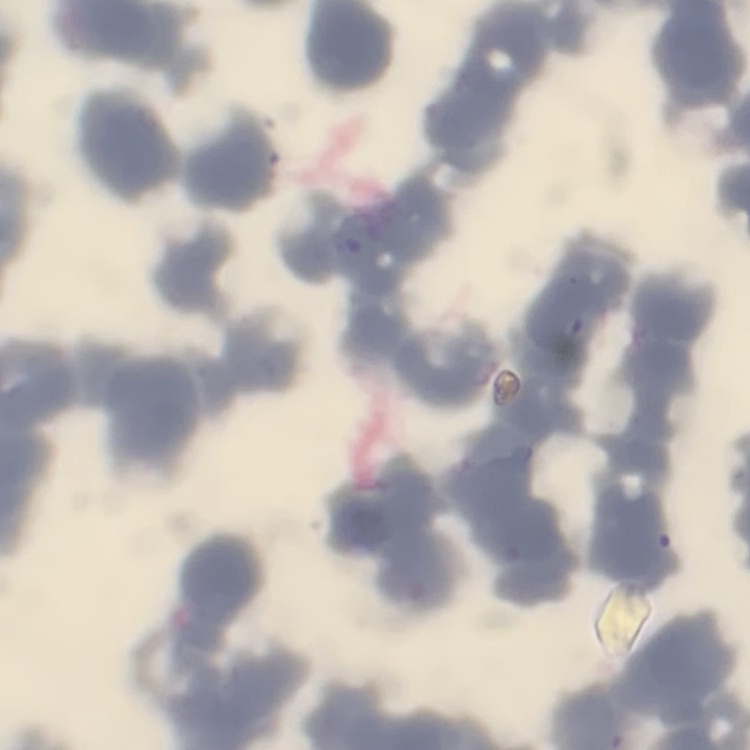

red blood cell morphology = rouleaux formation
stain = Field's or Giemsa
image type = one tile cut from a larger photomicrograph
preparation = thin blood smear